State which parasite is depicted.
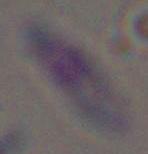

This is Toxoplasma gondii.

Captured at 1000x magnification. Photomicrograph.